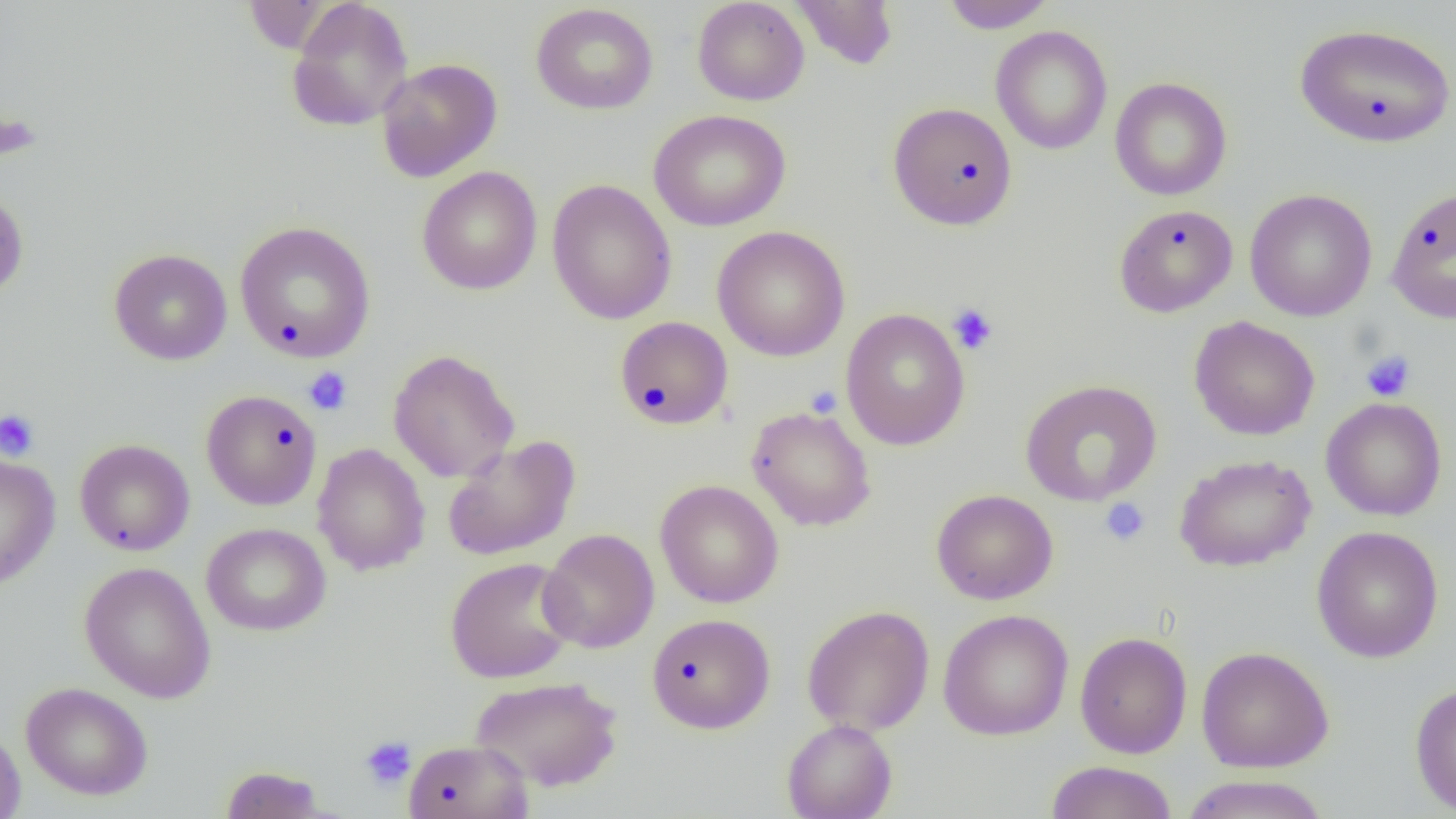
slide-level diagnosis = negative for blood parasites
image size = 1456×819 pixels
platelet locations = approximate bounding boxes as [x1, y1, x2, y2] in pixels: [947, 303, 999, 355], [1361, 350, 1415, 402], [303, 368, 352, 415], [0, 409, 40, 461], [1100, 497, 1150, 545], [360, 736, 417, 791]
preparation = thin blood smear
field of view = single
magnification = 1000x
modality = light microscopy
uninfected red blood cell locations = approximate bounding boxes as [x1, y1, x2, y2] in pixels: [692, 0, 809, 106], [791, 0, 900, 70], [938, 0, 1057, 33], [286, 1, 414, 132], [531, 3, 659, 115], [1293, 22, 1456, 148], [990, 25, 1113, 155], [376, 58, 502, 182], [1110, 77, 1232, 201], [887, 101, 1018, 230], [648, 109, 791, 232], [417, 166, 543, 295], [547, 179, 677, 325], [0, 185, 29, 302], [1385, 186, 1456, 324], [1245, 188, 1378, 321], [1114, 204, 1238, 318], [235, 221, 376, 363], [712, 225, 850, 361], [109, 248, 233, 365], [840, 308, 970, 451], [1189, 315, 1320, 441], [614, 316, 733, 430], [388, 349, 520, 483], [1019, 379, 1162, 506], [201, 389, 322, 510], [1320, 397, 1447, 521], [747, 406, 877, 531], [442, 435, 581, 562], [75, 439, 195, 556], [312, 443, 431, 576], [0, 453, 60, 590], [1175, 453, 1316, 571], [655, 480, 784, 608], [931, 488, 1059, 605], [201, 522, 331, 636], [1311, 526, 1444, 663], [539, 528, 659, 654], [444, 557, 578, 683], [79, 560, 217, 703], [801, 604, 935, 735], [937, 609, 1074, 740], [647, 613, 775, 733], [1074, 631, 1193, 759], [1195, 646, 1334, 772], [470, 675, 624, 791], [1409, 681, 1456, 816], [21, 682, 153, 800], [782, 718, 897, 819], [0, 726, 26, 819], [403, 738, 534, 819], [1044, 760, 1178, 819], [219, 765, 329, 818], [1178, 774, 1333, 818]